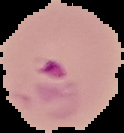
Cell region segmented out of the field of view; the surrounding area is masked to black. From a thin blood film. Malaria status: parasitized. Image is 124×133 pixels.